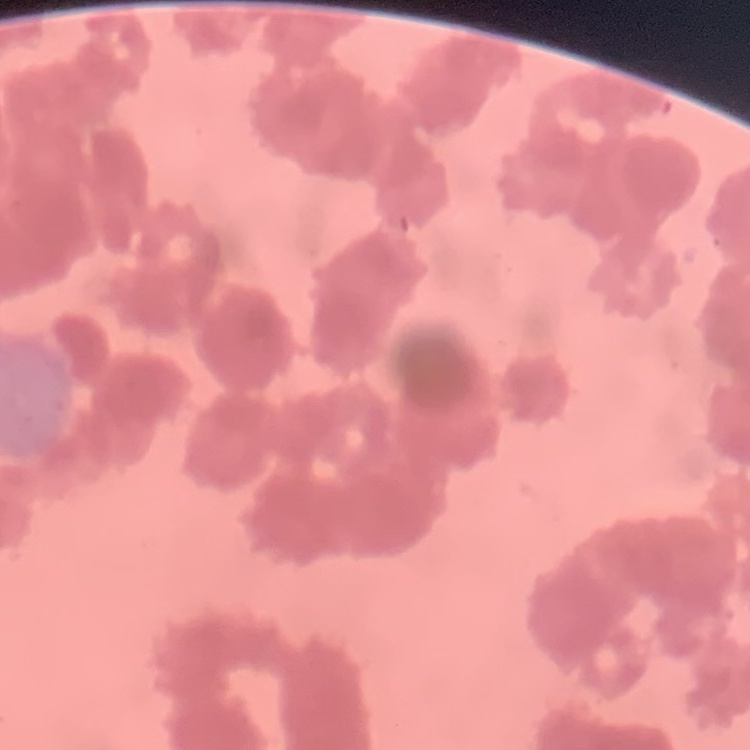

Summary:
  - Erythrocyte morphology: rouleaux formation
  - Image type: square crop of a larger photomicrograph
  - Stain: Field's or Giemsa
  - Preparation: thin blood film